Classify this cell by malaria status.
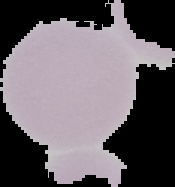

It is uninfected.

Summary:
  - Image type: segmented cell region on a black background
  - Image size: 175×187 pixels
  - Preparation: thin blood film